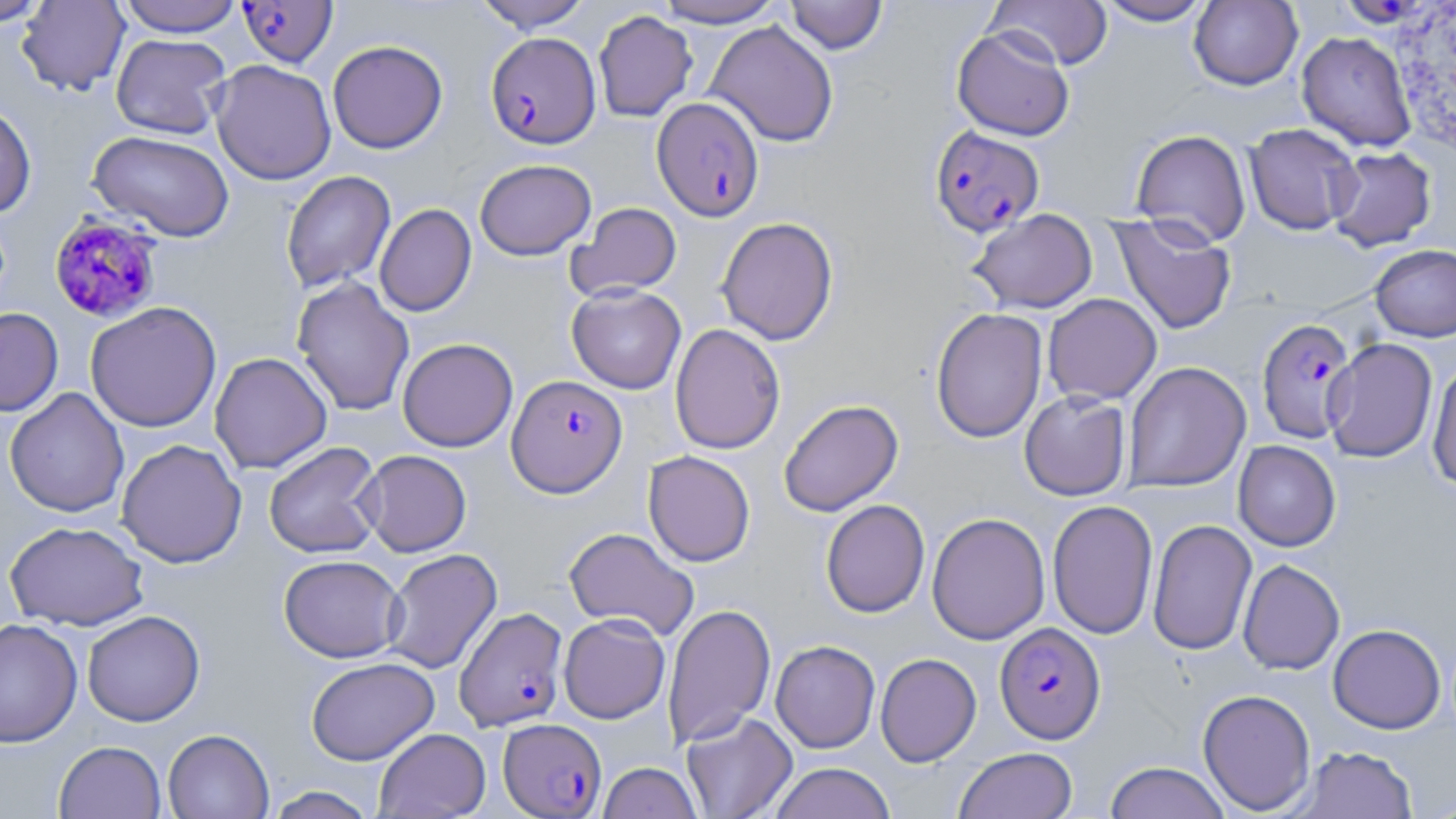

Approximate bounding boxes as named x1/y1/x2/y2 corners in pixels. Uninfected red blood cell locations: (x1=0, y1=0, x2=51, y2=26), (x1=17, y1=0, x2=131, y2=96), (x1=117, y1=0, x2=244, y2=36), (x1=473, y1=0, x2=592, y2=32), (x1=652, y1=0, x2=785, y2=28), (x1=987, y1=0, x2=1113, y2=69), (x1=1094, y1=0, x2=1214, y2=26), (x1=784, y1=1, x2=888, y2=54), (x1=1188, y1=1, x2=1303, y2=90), (x1=593, y1=10, x2=698, y2=122), (x1=705, y1=20, x2=839, y2=147), (x1=951, y1=25, x2=1075, y2=141), (x1=1296, y1=31, x2=1417, y2=152), (x1=111, y1=33, x2=232, y2=139), (x1=327, y1=40, x2=448, y2=154), (x1=210, y1=59, x2=337, y2=185), (x1=0, y1=102, x2=37, y2=219), (x1=1244, y1=122, x2=1362, y2=236), (x1=1131, y1=128, x2=1251, y2=247), (x1=87, y1=130, x2=235, y2=242), (x1=1326, y1=146, x2=1437, y2=252), (x1=475, y1=158, x2=596, y2=260), (x1=281, y1=170, x2=396, y2=293), (x1=566, y1=202, x2=682, y2=301), (x1=375, y1=203, x2=476, y2=317), (x1=967, y1=210, x2=1099, y2=314), (x1=1109, y1=214, x2=1237, y2=335), (x1=716, y1=217, x2=839, y2=345), (x1=1369, y1=244, x2=1456, y2=342), (x1=292, y1=277, x2=415, y2=416), (x1=567, y1=284, x2=686, y2=394), (x1=1043, y1=293, x2=1162, y2=405), (x1=85, y1=301, x2=222, y2=433), (x1=0, y1=307, x2=63, y2=416), (x1=930, y1=307, x2=1048, y2=444), (x1=669, y1=323, x2=786, y2=455), (x1=397, y1=337, x2=518, y2=452), (x1=1323, y1=338, x2=1438, y2=463), (x1=209, y1=352, x2=332, y2=474), (x1=1427, y1=359, x2=1456, y2=490), (x1=1123, y1=361, x2=1251, y2=493), (x1=4, y1=387, x2=129, y2=518), (x1=1019, y1=390, x2=1131, y2=501), (x1=778, y1=399, x2=903, y2=517), (x1=116, y1=439, x2=247, y2=568), (x1=263, y1=441, x2=384, y2=558), (x1=1233, y1=441, x2=1341, y2=552), (x1=358, y1=449, x2=471, y2=556), (x1=643, y1=451, x2=756, y2=567), (x1=820, y1=499, x2=930, y2=618), (x1=1047, y1=499, x2=1158, y2=639), (x1=926, y1=512, x2=1051, y2=645), (x1=1147, y1=519, x2=1257, y2=656), (x1=4, y1=520, x2=149, y2=630), (x1=564, y1=527, x2=700, y2=640), (x1=381, y1=548, x2=502, y2=675), (x1=278, y1=554, x2=405, y2=662), (x1=1237, y1=559, x2=1345, y2=675), (x1=663, y1=603, x2=775, y2=748), (x1=82, y1=610, x2=204, y2=726), (x1=558, y1=613, x2=670, y2=724), (x1=0, y1=618, x2=83, y2=748), (x1=1328, y1=623, x2=1445, y2=733), (x1=770, y1=640, x2=880, y2=753), (x1=875, y1=653, x2=981, y2=766), (x1=306, y1=657, x2=439, y2=765), (x1=1197, y1=689, x2=1316, y2=814), (x1=681, y1=711, x2=798, y2=819), (x1=374, y1=728, x2=490, y2=818), (x1=163, y1=729, x2=274, y2=819), (x1=54, y1=740, x2=166, y2=818), (x1=1295, y1=745, x2=1418, y2=818), (x1=953, y1=746, x2=1078, y2=819), (x1=597, y1=761, x2=703, y2=819), (x1=1104, y1=761, x2=1231, y2=819), (x1=767, y1=762, x2=897, y2=819), (x1=264, y1=786, x2=378, y2=819), (x1=1421, y1=791, x2=1456, y2=818). Plasmodium falciparum-infected red blood cell locations: (x1=237, y1=1, x2=338, y2=68), (x1=485, y1=32, x2=600, y2=149), (x1=651, y1=96, x2=764, y2=221), (x1=929, y1=125, x2=1046, y2=237), (x1=49, y1=211, x2=165, y2=322), (x1=1257, y1=318, x2=1357, y2=444), (x1=507, y1=374, x2=627, y2=497), (x1=454, y1=606, x2=568, y2=730), (x1=994, y1=622, x2=1106, y2=744), (x1=498, y1=718, x2=606, y2=817). Slide-level diagnosis: Plasmodium falciparum. Thin blood smear. One field of a larger specimen. 1000x magnification. Light microscopy. May-Grünwald-Giemsa stain. Image is 1456×819 pixels.